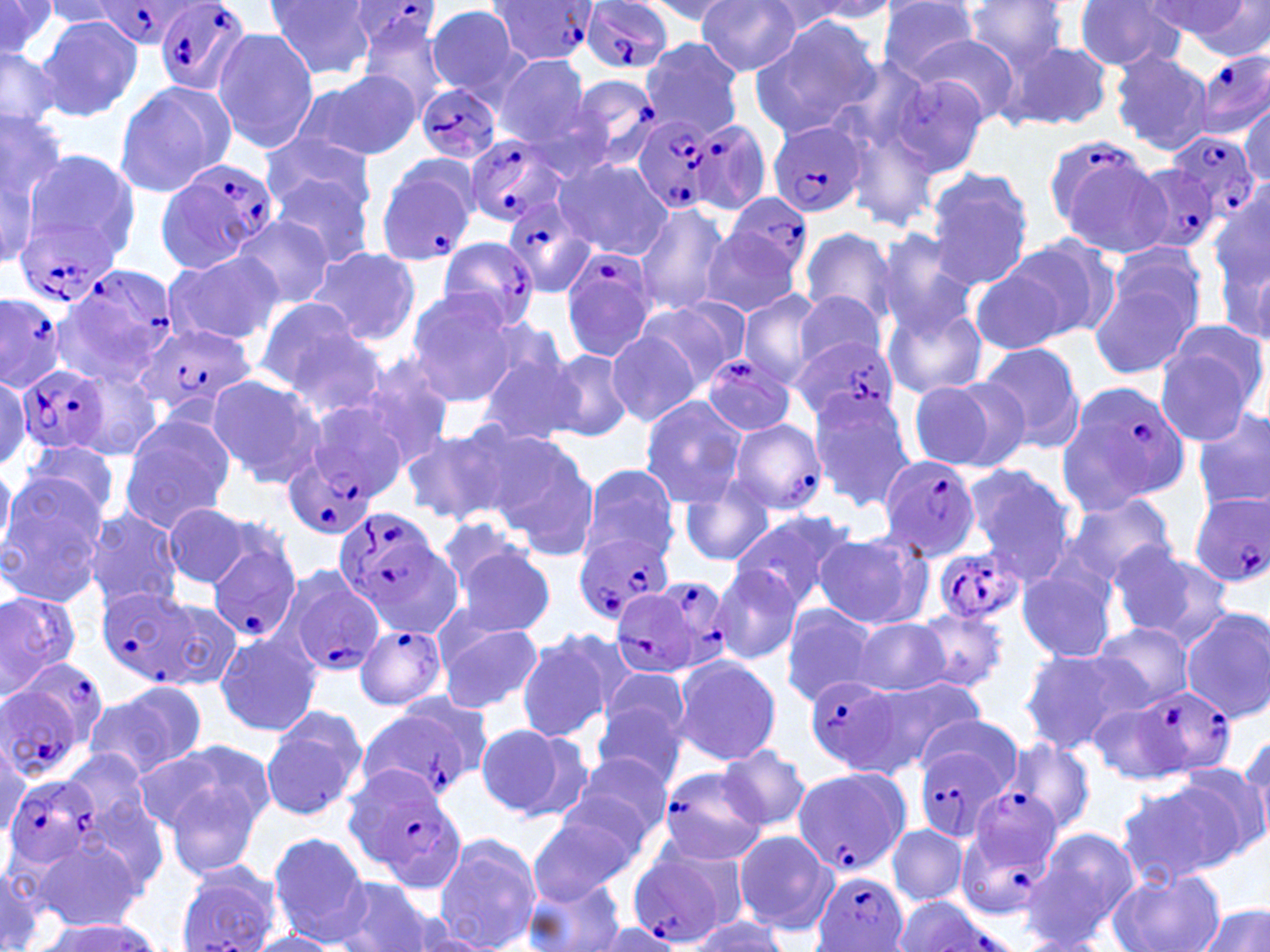
slide-level diagnosis = Plasmodium falciparum
uninfected red blood cell locations (subset) = approximate bounding boxes as (x1,y1)-(x2,y2) corner pairs in pixels: (266,0)-(377,81), (878,0)-(982,80), (959,0)-(1076,73), (1073,0)-(1188,71), (1145,0)-(1254,46), (0,1)-(57,58), (640,1)-(742,23), (697,1)-(802,76), (43,2)-(130,28), (759,2)-(877,36), (792,2)-(904,23), (1179,3)-(1270,62), (426,5)-(527,100), (35,15)-(142,124), (749,17)-(882,138), (357,18)-(454,118), (211,30)-(320,151), (906,31)-(1022,125), (639,36)-(743,138), (1001,40)-(1113,132), (0,43)-(64,133), (1110,49)-(1214,157), (1195,49)-(1270,140), (495,56)-(594,145), (297,71)-(420,162), (885,73)-(993,177), (114,80)-(234,199), (1239,100)-(1269,189), (0,105)-(69,231), (262,133)-(378,226), (0,137)-(49,271), (21,148)-(139,270), (555,158)-(672,260), (267,170)-(377,271), (923,170)-(1035,291), (1212,191)-(1269,341), (633,201)-(730,318), (232,217)-(334,310), (798,226)-(897,327), (872,229)-(979,337), (699,236)-(805,318), (1002,236)-(1120,342), (310,246)-(425,346), (1090,246)-(1212,378), (163,249)-(284,347), (280,250)-(413,407), (972,264)-(1073,356), (404,289)-(521,403), (791,290)-(890,373), (738,291)-(824,386), (254,301)-(377,404), (638,301)-(743,389), (882,301)-(988,398), (1157,317)-(1269,430), (606,331)-(704,427), (976,342)-(1086,456), (472,343)-(581,447), (542,348)-(635,441), (352,356)-(456,466), (69,368)-(166,463), (0,371)-(30,471), (204,375)-(326,488), (908,376)-(1026,473), (807,390)-(917,509), (304,395)-(418,497), (638,396)-(746,509), (1194,407)-(1270,512), (119,417)-(233,531), (399,422)-(525,528), (484,431)-(601,555), (17,440)-(122,528), (961,464)-(1079,582), (578,465)-(677,566), (0,466)-(16,559), (680,478)-(774,567), (0,482)-(107,608), (1062,492)-(1179,587), (162,502)-(259,589), (82,506)-(185,614), (729,508)-(858,612), (433,515)-(536,601), (813,532)-(930,631), (1104,540)-(1223,643), (450,545)-(555,639), (1015,559)-(1121,665), (711,564)-(802,664), (0,588)-(81,693), (150,597)-(244,690), (779,603)-(880,706), (910,606)-(1008,693), (1180,607)-(1270,722), (851,617)-(952,697), (437,620)-(544,713), (1089,622)-(1194,711), (215,630)-(322,737), (515,630)-(620,742), (498,635)-(607,821), (1019,648)-(1141,750), (672,653)-(782,766), (598,669)-(692,752), (863,674)-(986,772), (88,683)-(206,781), (591,699)-(689,788), (1087,702)-(1186,783), (260,709)-(366,823), (914,713)-(1022,795), (474,721)-(589,823), (1239,729)-(1270,848), (996,734)-(1097,837), (136,739)-(270,840), (719,744)-(811,832), (567,751)-(674,843), (537,760)-(663,911), (1167,762)-(1266,867), (165,771)-(267,882), (1117,778)-(1242,884), (71,785)-(173,902), (525,811)-(633,904), (886,825)-(968,907), (1022,827)-(1133,949), (733,829)-(835,935), (268,831)-(371,942), (434,833)-(542,950), (29,834)-(145,930), (0,860)-(50,952), (175,865)-(280,951), (1110,869)-(1224,952), (331,876)-(438,952), (523,876)-(627,952), (1197,905)-(1268,952), (685,913)-(791,952), (31,916)-(164,951), (590,919)-(683,952), (247,932)-(343,952)
Plasmodium falciparum-infected red blood cell locations (subset) = approximate bounding boxes as (x1,y1)-(x2,y2) corner pairs in pixels: (153,0)-(252,98), (583,1)-(672,75), (342,2)-(441,55), (90,3)-(197,48), (569,74)-(664,171), (415,83)-(500,165), (633,117)-(720,214), (688,118)-(773,217), (768,118)-(868,219), (465,133)-(575,229), (1166,134)-(1259,224), (1041,135)-(1168,250), (374,154)-(481,269), (158,158)-(279,272), (1131,164)-(1225,260), (726,194)-(810,281), (501,196)-(597,301), (13,218)-(115,306), (434,238)-(540,330), (560,248)-(658,363), (56,269)-(176,387), (0,292)-(67,388), (138,322)-(258,422), (794,336)-(900,423), (704,355)-(798,436), (16,363)-(109,453), (1066,379)-(1193,506), (726,418)-(828,516), (284,454)-(378,540), (878,455)-(981,562), (1190,494)-(1270,588), (332,505)-(453,628), (574,530)-(677,624), (206,538)-(302,645), (932,544)-(1026,625), (282,569)-(386,678), (652,571)-(742,676), (96,587)-(202,685), (608,587)-(707,680), (354,624)-(448,711), (11,655)-(113,759), (805,676)-(903,773), (1128,684)-(1238,779), (1,685)-(83,783), (358,704)-(481,802), (914,747)-(1012,846), (655,764)-(770,865), (791,766)-(908,876), (342,767)-(461,879), (2,774)-(97,870), (959,791)-(1063,906), (628,848)-(735,948), (815,872)-(909,952), (891,897)-(1011,951)
magnification = 1000x
modality = optical microscopy
image size = 1270×952 pixels
platelet locations = approximate bounding boxes as (x1,y1)-(x2,y2) corner pairs in pixels: (1216,64)-(1239,91)
stain = May-Grünwald-Giemsa
field of view = single
preparation = thin blood smear